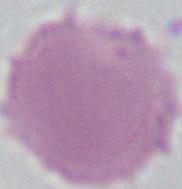
A red blood cell is shown. 1000x magnification. Photomicrograph.